Report the malaria status of this cell.
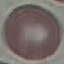

Uninfected.

Summary:
  - Capture: smartphone through the microscope eyepiece
  - Image type: cell patch, automatically extracted from a larger field of view and resized to 64 × 64 pixels
  - Preparation: thin blood smear
  - Stain: Giemsa